Identify the parasite.
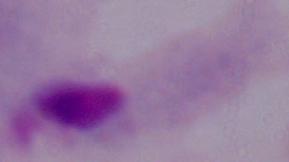

This is a trichomonad.

modality = photomicrograph
magnification = 1000x